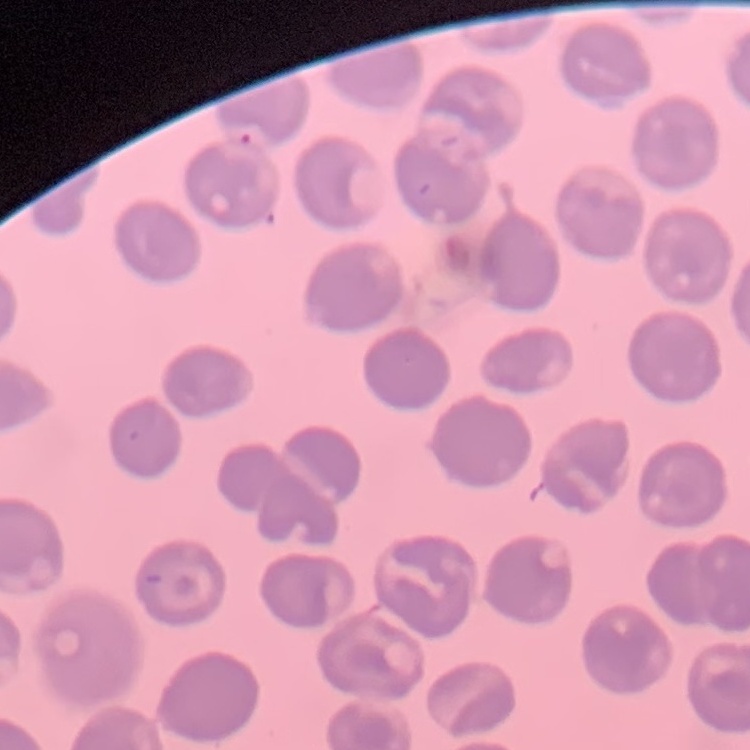

The red blood cells exhibit no rouleaux formation. One tile cut from a larger photomicrograph. Thin blood film. Field's or Giemsa stain.